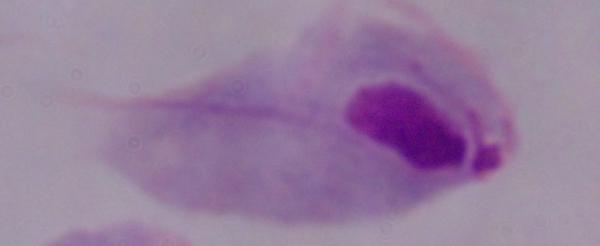

Summary:
  - Magnification: 1000x
  - Identification: trichomonad
  - Modality: micrograph